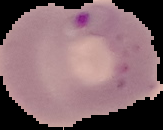

Summary:
  - Preparation: thin blood film
  - Image size: 163×130 pixels
  - Result: malaria parasites detected
  - Image type: cell region segmented out of the field of view; surrounding area masked to black